Classify the preparation.
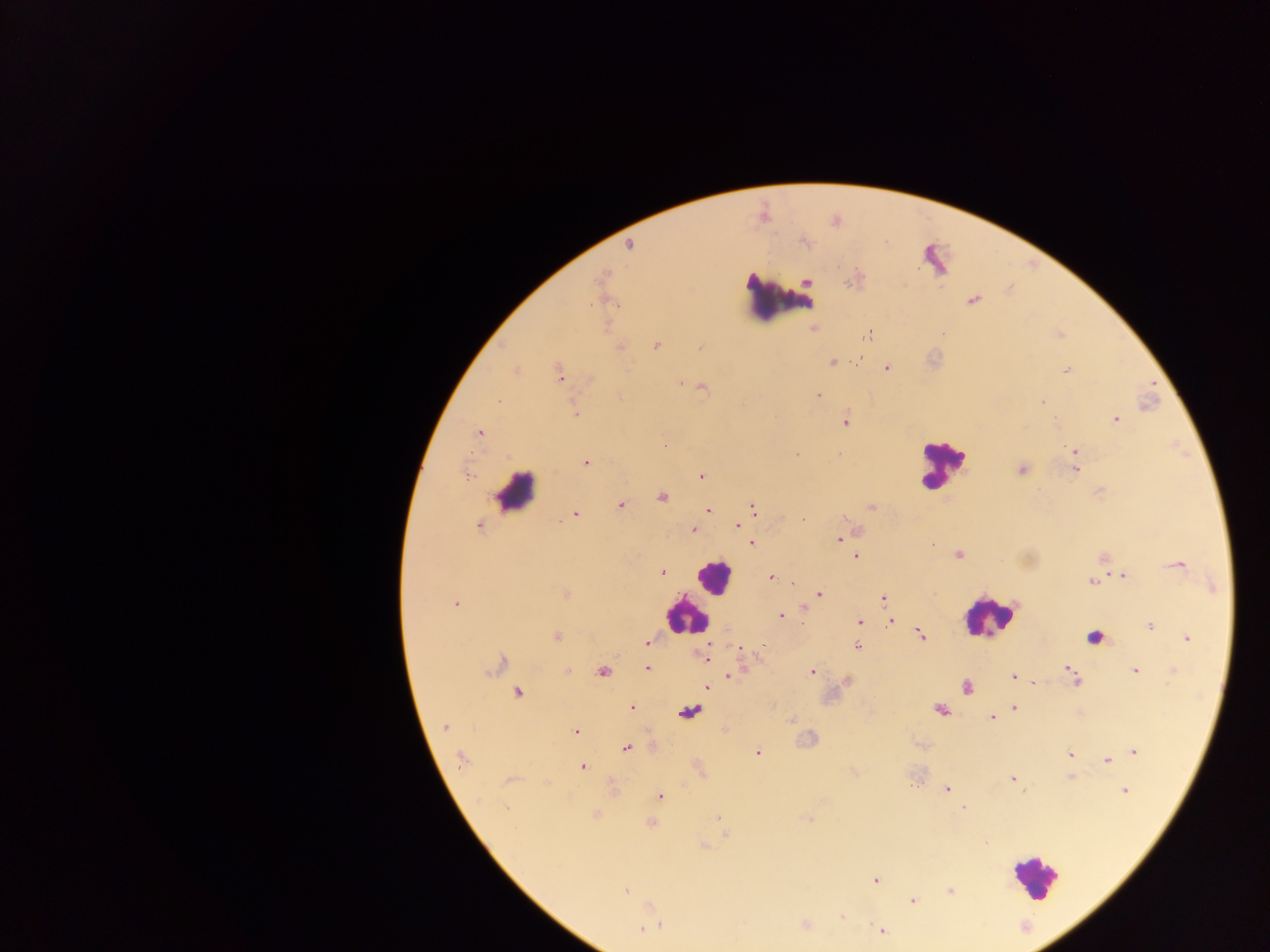
Thick blood smear.

image size = 1270×952 pixels
field of view = single
Plasmodium parasite locations = approximate centers as {x, y} in pixels: {629, 245}, {601, 277}, {808, 281}, {973, 300}, {942, 334}, {868, 335}, {620, 346}, {656, 346}, {832, 362}, {886, 368}, {1066, 371}, {559, 373}, {680, 384}, {703, 387}, {818, 396}, {498, 401}, {1042, 402}, {575, 414}, {1116, 420}, {844, 421}, {479, 433}, {665, 444}, {1074, 451}, {796, 454}, {586, 462}, {1022, 469}, {1076, 469}, {467, 474}, {701, 476}, {662, 496}, {620, 506}, {753, 507}, {871, 507}, {708, 510}, {574, 514}, {479, 525}, {737, 526}, {693, 529}, {839, 539}, {751, 543}, {959, 555}, {857, 556}, {1177, 565}, {662, 572}, {1124, 576}, {771, 577}, {1091, 581}, {792, 583}, {565, 593}, {818, 595}, {883, 598}, {455, 603}, {781, 616}, {860, 621}, {891, 621}, {1149, 626}, {921, 635}, {556, 636}, {1187, 638}, {647, 641}, {764, 645}, {857, 647}, {740, 649}, {705, 657}, {500, 663}, {647, 668}, {1068, 669}, {567, 670}, {1135, 670}, {603, 672}, {812, 673}, {1072, 674}, {729, 676}, {1013, 677}, {1076, 681}, {1034, 683}, {707, 687}, {966, 687}, {518, 692}, {632, 707}, {1014, 708}, {940, 709}, {992, 717}, {445, 727}, {575, 731}, {625, 748}, {1135, 751}, {758, 753}, {1070, 755}, {462, 760}, {1107, 760}, {582, 767}, {1013, 779}, {946, 789}, {1125, 791}, {660, 796}, {505, 808}, {963, 808}, {717, 818}, {652, 823}, {876, 880}, {949, 890}, {626, 891}, {913, 901}, {841, 917}, {659, 925}, {651, 927}, {644, 928}, {881, 930}
capture = mobile-phone photograph through a microscope
country = Ghana
leukocyte locations = approximate centers as {x, y} in pixels: {782, 298}, {942, 464}, {515, 491}, {712, 577}, {987, 615}, {684, 616}, {1095, 639}, {1034, 876}